Report the malaria status of this cell.
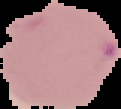
Parasitized.

image type = segmented cell region with the area outside set to black
image size = 121×109 pixels
preparation = thin blood smear